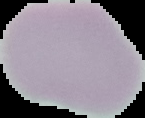

Summary:
  - Image type: segmented cell region with the area outside set to black
  - Image size: 145×118 pixels
  - Preparation: thin blood film
  - Malaria status: uninfected